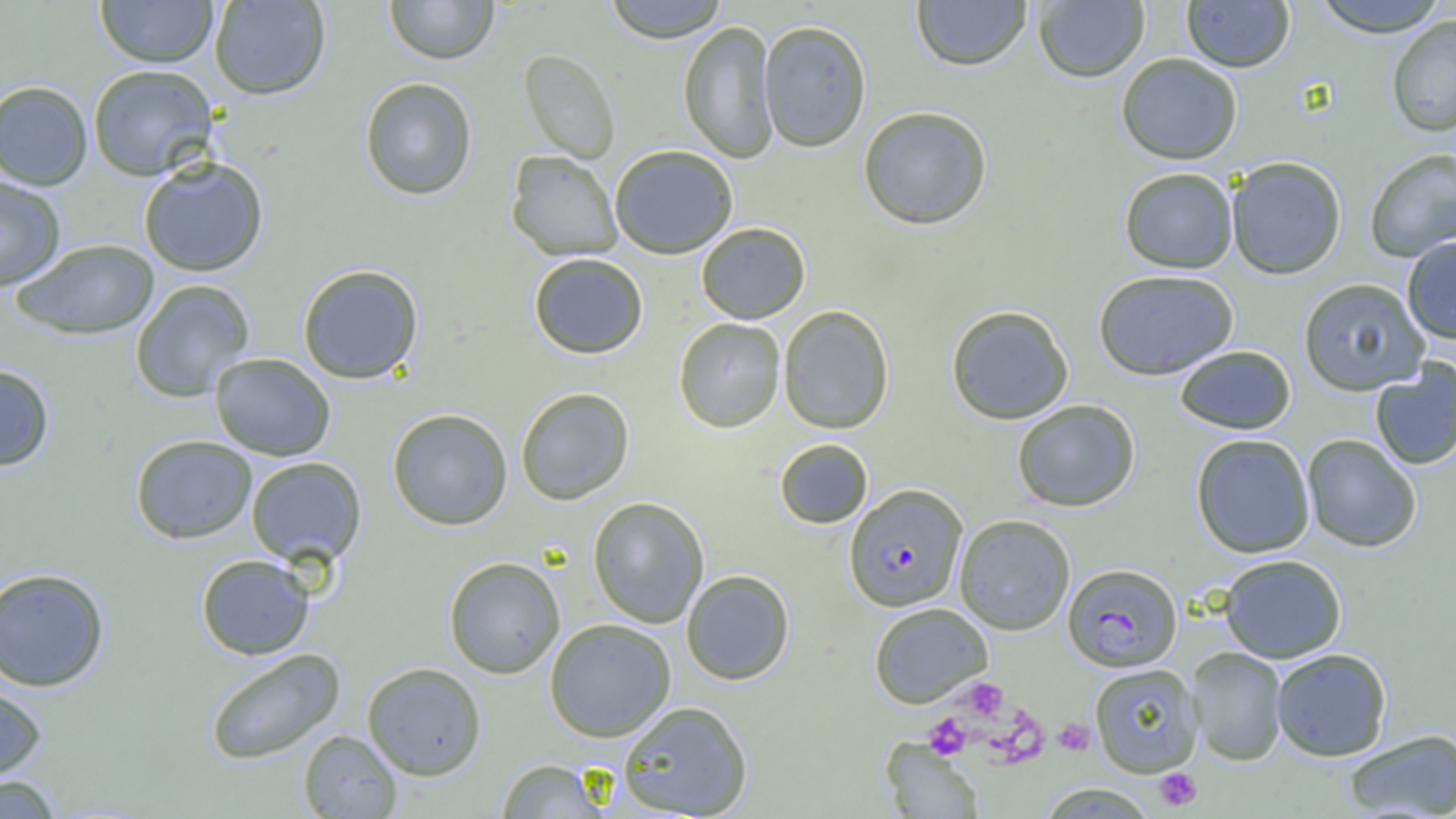

Summary:
  - Coordinate format: approximate bounding boxes as (x1,y1)-(x2,y2) corner pairs in pixels
  - Uninfected red blood cell locations (subset): (95,0)-(218,68), (209,0)-(331,101), (384,0)-(500,65), (602,0)-(730,43), (910,0)-(1032,71), (1033,0)-(1150,83), (1309,0)-(1450,37), (1181,1)-(1296,73), (1386,14)-(1456,138), (758,19)-(872,152), (678,20)-(779,163), (518,49)-(620,164), (1116,52)-(1243,165), (87,64)-(218,181), (359,77)-(477,201), (0,80)-(93,190), (857,105)-(993,231), (609,144)-(738,259), (1364,148)-(1456,263), (505,150)-(623,261), (1225,155)-(1347,280), (138,156)-(269,277), (1119,167)-(1239,274), (0,175)-(66,291), (696,222)-(811,324), (1401,236)-(1456,345), (10,239)-(160,340), (528,252)-(649,359), (297,263)-(425,385), (1092,269)-(1239,380), (1297,277)-(1430,396), (129,279)-(255,403), (945,304)-(1074,425), (778,305)-(895,434), (673,317)-(786,433), (1174,345)-(1296,434), (209,353)-(336,461), (1369,360)-(1456,471), (0,363)-(55,471), (515,387)-(635,505), (1011,399)-(1141,513), (386,408)-(513,530), (1190,433)-(1316,558), (130,434)-(258,545), (1301,434)-(1422,553), (774,438)-(873,529), (245,456)-(367,567), (587,496)-(710,628), (953,514)-(1076,635), (196,554)-(315,660), (1218,554)-(1347,664), (443,556)-(566,679), (0,567)-(110,692), (681,569)-(795,685), (868,602)-(993,709), (544,618)-(677,742), (1186,647)-(1288,766), (205,648)-(346,765), (1270,648)-(1393,761), (361,662)-(487,780), (1088,663)-(1204,778), (0,680)-(48,783), (617,700)-(754,818), (1342,729)-(1456,818), (298,730)-(403,818), (494,758)-(612,817), (0,774)-(66,818), (1035,783)-(1160,819)
  - Platelet locations (subset): (963,678)-(1008,721), (923,713)-(971,758), (1053,719)-(1096,756), (1154,767)-(1202,811)
  - Plasmodium falciparum-infected red blood cell locations: (843,484)-(968,612), (1062,563)-(1183,672)
  - Slide-level diagnosis: Plasmodium falciparum
  - Image size: 1456×819 pixels
  - Field of view: one of a larger specimen
  - Preparation: thin blood film
  - Magnification: 1000x
  - Modality: light microscopy